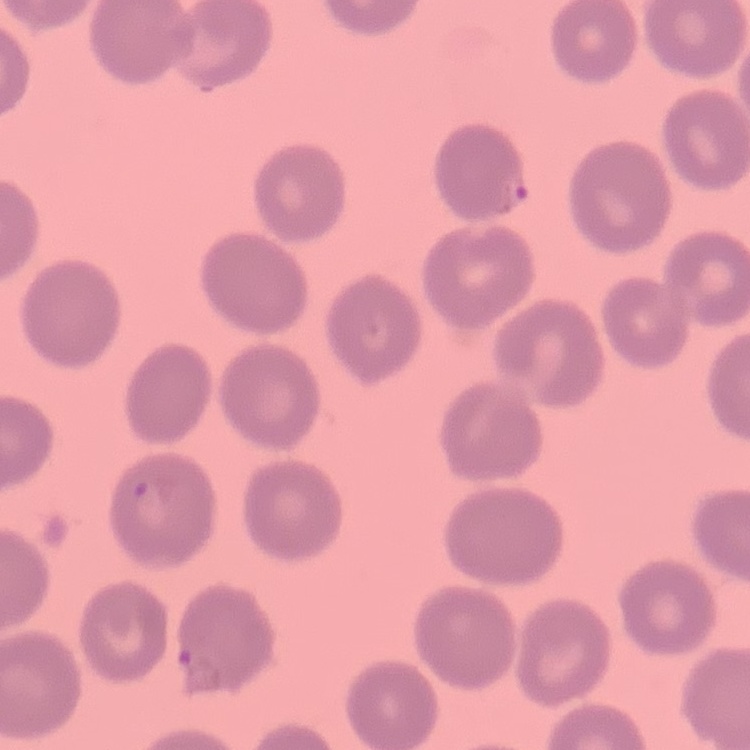

The erythrocytes show no rouleaux formation. Field's or Giemsa stain. Square crop of a larger photomicrograph. Thin blood film.